Locate every Plasmodium falciparum-infected red blood cell.
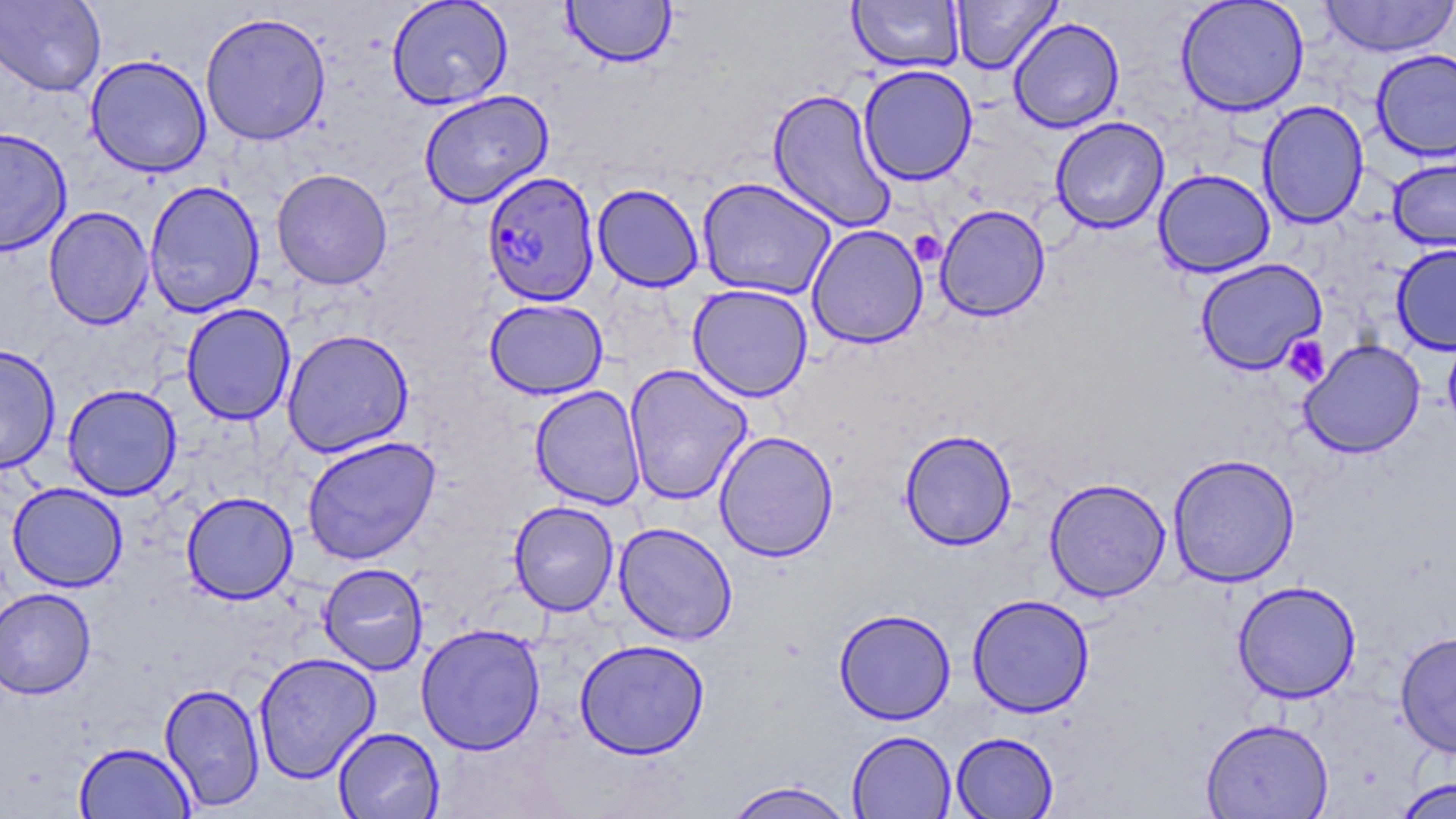
Approximate bounding boxes as (x1, y1, x2, y2) in pixels.
Plasmodium falciparum-infected red blood cells: (482, 171, 600, 307).

slide-level diagnosis = Plasmodium falciparum
stain = May-Grünwald-Giemsa
platelet locations = approximate bounding boxes as (x1, y1, x2, y2) in pixels: (910, 230, 946, 267), (1283, 335, 1330, 386)
uninfected red blood cell locations = approximate bounding boxes as (x1, y1, x2, y2) in pixels: (0, 0, 106, 96), (387, 0, 513, 110), (951, 0, 1062, 74), (1174, 0, 1310, 117), (1318, 0, 1456, 58), (561, 1, 677, 68), (848, 1, 965, 73), (200, 11, 331, 146), (1008, 16, 1125, 133), (1371, 49, 1456, 162), (84, 54, 212, 178), (858, 64, 978, 185), (767, 87, 896, 232), (418, 90, 554, 208), (1258, 99, 1369, 230), (1050, 116, 1170, 234), (0, 127, 72, 254), (1387, 156, 1456, 252), (271, 168, 393, 289), (1153, 168, 1275, 277), (696, 177, 838, 300), (144, 180, 265, 318), (591, 183, 705, 292), (934, 204, 1051, 322), (43, 206, 155, 330), (806, 224, 928, 349), (1391, 243, 1456, 355), (1194, 258, 1327, 375), (687, 284, 813, 402), (484, 298, 609, 399), (181, 303, 296, 425), (281, 328, 414, 458), (1299, 338, 1426, 458), (1, 345, 61, 474), (624, 363, 753, 504), (62, 384, 182, 501), (530, 385, 646, 509), (899, 429, 1017, 550), (714, 430, 839, 561), (301, 436, 441, 565), (1168, 453, 1300, 587), (1044, 477, 1170, 601), (8, 482, 128, 592), (181, 491, 298, 604), (508, 501, 619, 616), (613, 522, 738, 644), (318, 562, 429, 675), (1232, 580, 1362, 703), (0, 587, 96, 699), (967, 594, 1095, 717), (834, 608, 956, 725), (416, 623, 546, 755), (1395, 631, 1456, 758), (574, 639, 710, 760), (254, 651, 381, 783), (159, 682, 265, 811), (1200, 717, 1334, 819), (332, 726, 445, 818), (847, 730, 956, 818), (951, 732, 1059, 818), (73, 741, 196, 819), (1393, 776, 1456, 819), (723, 780, 858, 819)
magnification = 1000x
preparation = thin blood smear
field of view = single
modality = light microscopy
image size = 1456×819 pixels